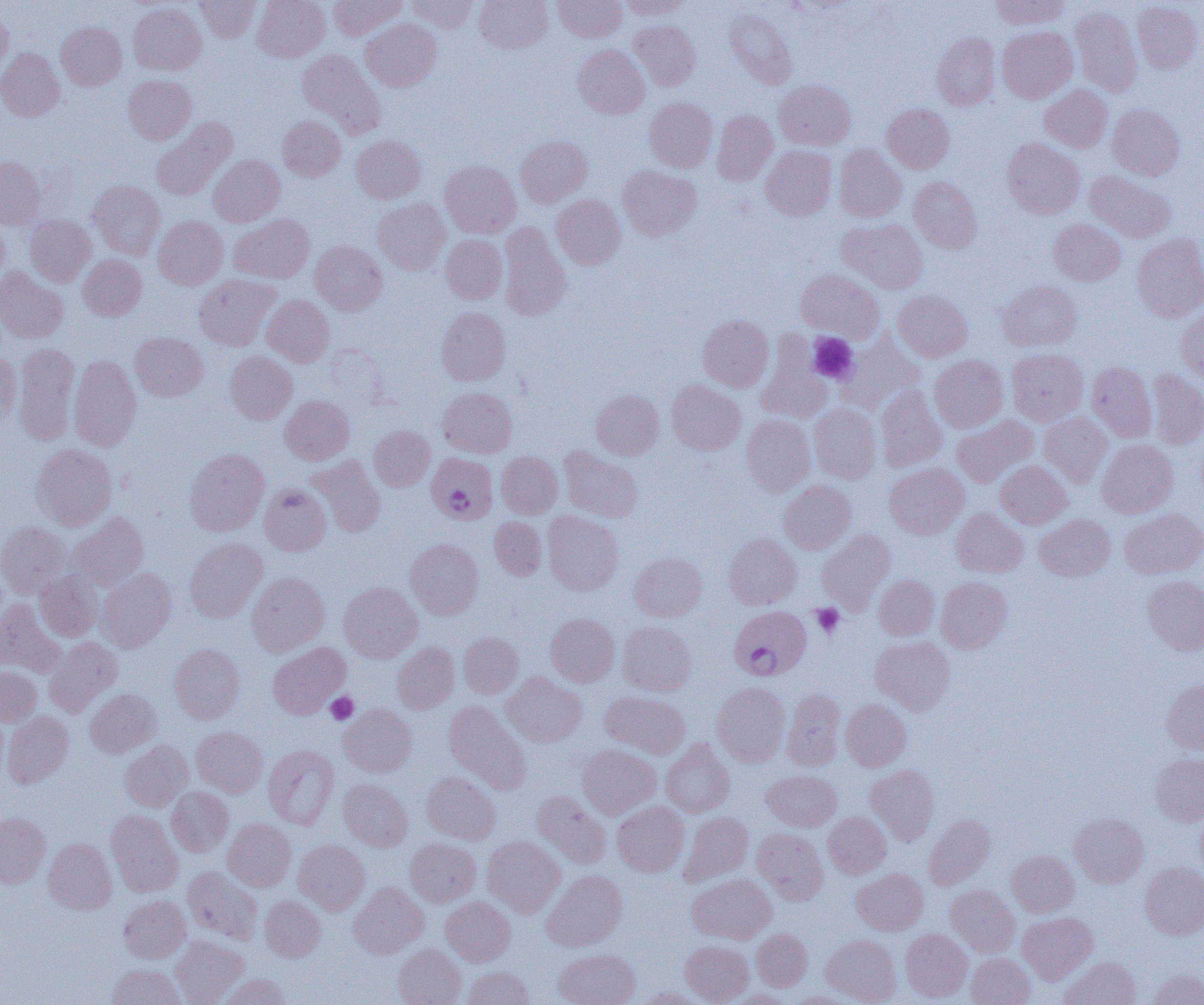
Approximate bounding boxes as (x1,y1)-(x2,y2) corner pairs in pixels. Uninfected red blood cell locations: (194,0)-(261,43), (252,0)-(329,62), (329,0)-(406,39), (407,0)-(478,33), (475,0)-(552,54), (552,0)-(626,42), (621,0)-(693,19), (990,0)-(1070,29), (1132,1)-(1203,74), (128,3)-(206,75), (0,7)-(12,77), (724,7)-(797,89), (1070,7)-(1142,96), (361,18)-(441,91), (628,20)-(701,91), (56,22)-(126,90), (997,26)-(1077,103), (932,32)-(1000,110), (573,44)-(650,119), (0,48)-(65,122), (297,49)-(384,137), (123,75)-(197,145), (774,79)-(855,150), (1040,84)-(1112,152), (644,97)-(717,172), (881,103)-(954,173), (1107,104)-(1185,181), (712,109)-(777,186), (277,115)-(346,181), (152,119)-(234,200), (351,135)-(426,203), (515,135)-(592,208), (1002,138)-(1085,219), (834,144)-(907,222), (761,146)-(836,220), (209,154)-(285,227), (0,157)-(45,229), (440,160)-(521,238), (618,165)-(701,241), (1085,170)-(1176,242), (909,176)-(982,253), (88,180)-(165,259), (551,194)-(626,270), (372,198)-(450,275), (229,214)-(314,283), (25,215)-(96,286), (153,216)-(228,289), (0,218)-(9,290), (837,218)-(927,293), (1049,219)-(1125,286), (498,221)-(571,321), (1131,233)-(1204,322), (441,234)-(507,304), (310,241)-(387,315), (78,254)-(146,320), (0,267)-(68,343), (795,269)-(884,342), (194,274)-(280,350), (997,280)-(1082,351), (893,290)-(972,362), (262,295)-(334,367), (436,306)-(511,386), (1176,307)-(1204,382), (697,315)-(774,392), (130,332)-(208,401), (837,333)-(924,414), (756,335)-(831,423), (14,343)-(80,444), (324,345)-(389,406), (1007,348)-(1088,426), (0,351)-(21,424), (225,351)-(297,424), (929,355)-(1008,432), (69,356)-(141,451), (1087,361)-(1157,442), (1146,369)-(1204,450), (666,380)-(745,455), (875,385)-(948,472), (437,386)-(517,457), (591,389)-(664,460), (280,395)-(354,465), (809,403)-(881,483), (1039,412)-(1112,487), (741,414)-(815,496), (952,414)-(1038,487), (369,425)-(435,491), (1097,439)-(1178,518), (31,444)-(117,531), (559,447)-(643,523), (185,448)-(269,536), (496,451)-(563,518), (307,455)-(386,537), (995,460)-(1072,529), (884,462)-(969,540), (779,481)-(856,554), (259,483)-(331,555), (951,507)-(1028,577), (1120,508)-(1204,579), (543,510)-(623,595), (68,513)-(149,590), (1035,514)-(1115,581), (489,516)-(547,580), (0,521)-(70,598), (817,529)-(896,613), (724,533)-(801,609), (184,538)-(268,622), (405,539)-(483,619), (629,552)-(707,621), (97,568)-(176,652), (35,570)-(103,642), (246,572)-(329,656), (874,574)-(939,640), (1142,575)-(1204,655), (935,576)-(1012,653), (338,581)-(423,662), (0,599)-(66,677), (545,613)-(620,686), (618,621)-(697,696), (458,632)-(523,698), (870,636)-(956,715), (44,637)-(123,717), (268,642)-(350,719), (392,642)-(459,713), (169,644)-(244,723), (0,666)-(41,726), (501,671)-(587,747), (1161,679)-(1204,754), (712,682)-(790,767), (85,688)-(161,758), (782,688)-(846,770), (600,691)-(691,759), (841,699)-(911,771), (444,700)-(532,794), (339,704)-(416,777), (2,712)-(73,788), (191,726)-(268,797), (661,739)-(735,817), (120,740)-(193,812), (263,744)-(339,829), (577,744)-(661,819), (1150,753)-(1204,826), (865,764)-(939,845), (762,769)-(841,831), (421,771)-(500,844), (338,778)-(412,851), (166,786)-(234,856), (531,790)-(611,869), (612,801)-(689,877), (1195,808)-(1204,880), (106,810)-(183,896), (679,811)-(753,886), (823,812)-(891,879), (1069,812)-(1148,888), (0,813)-(50,887), (924,814)-(995,889), (223,819)-(296,891), (753,828)-(828,904), (482,836)-(565,917), (43,838)-(117,914), (405,838)-(481,906), (294,840)-(370,915), (1007,849)-(1079,917), (1140,861)-(1204,939), (183,866)-(263,945), (852,868)-(928,935), (542,870)-(627,951), (687,874)-(776,943), (349,882)-(429,959), (945,884)-(1020,956), (118,895)-(191,963), (260,896)-(326,962), (441,896)-(515,966), (1017,911)-(1098,984), (900,928)-(972,1002), (752,929)-(812,990), (820,934)-(901,1004), (170,936)-(249,1005), (680,940)-(753,1004), (393,943)-(466,1005), (553,948)-(640,1005), (966,953)-(1035,1005), (1060,956)-(1141,1005), (107,963)-(186,1005), (461,965)-(534,1005), (1147,968)-(1204,1005), (217,973)-(293,1005), (637,987)-(707,1005), (725,989)-(793,1004), (786,991)-(857,1004). Plasmodium falciparum-infected red blood cell locations: (426,452)-(498,524), (730,606)-(811,681). Platelet locations: (807,333)-(858,384), (811,604)-(844,638), (326,692)-(359,724). Slide-level diagnosis: Plasmodium falciparum. One field of a larger specimen. Image is 1204×1005 pixels. Light microscopy. Thin blood smear. 1000x magnification.